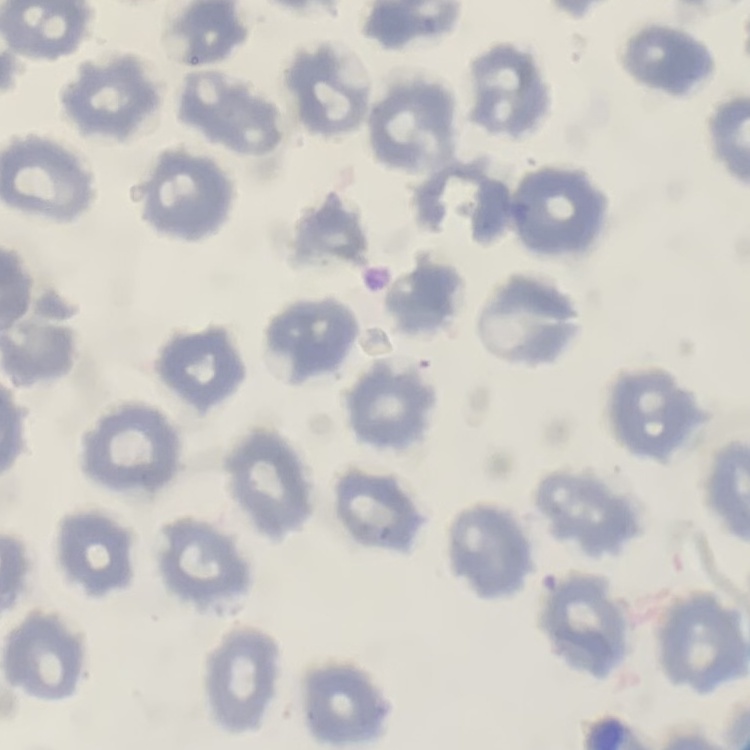

red blood cell morphology = no rouleaux formation
image type = one tile cut from a larger photomicrograph
stain = Field's or Giemsa
preparation = thin blood film